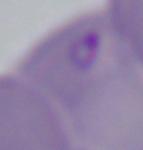

identification = Babesia
magnification = 1000x
modality = micrograph